State which parasite is depicted.
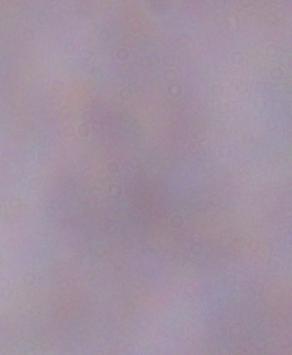

A trypanosome.

Photomicrograph. Captured at 1000x magnification.